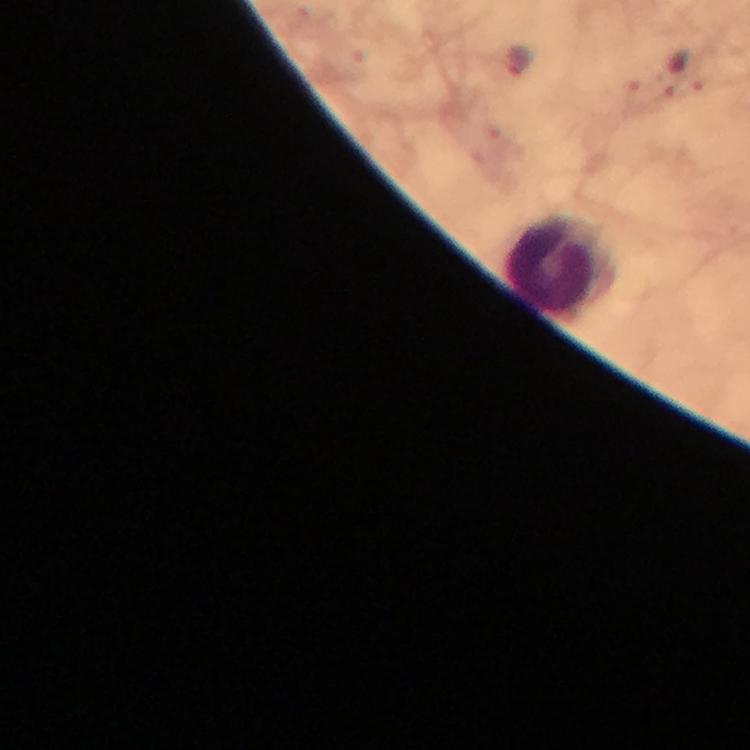
Approximate centers as {x, y} in pixels. Malaria parasite locations: {518, 62}. Leukocyte locations: {562, 267}. At 100x magnification. Immersion oil was used. Thick blood smear. Giemsa-stained preparation. Smartphone photograph taken through a microscope. Cropped region of a single field of view. From a diagnostic examination for malaria. Image is 750×750 pixels.